Point out leukocytes.
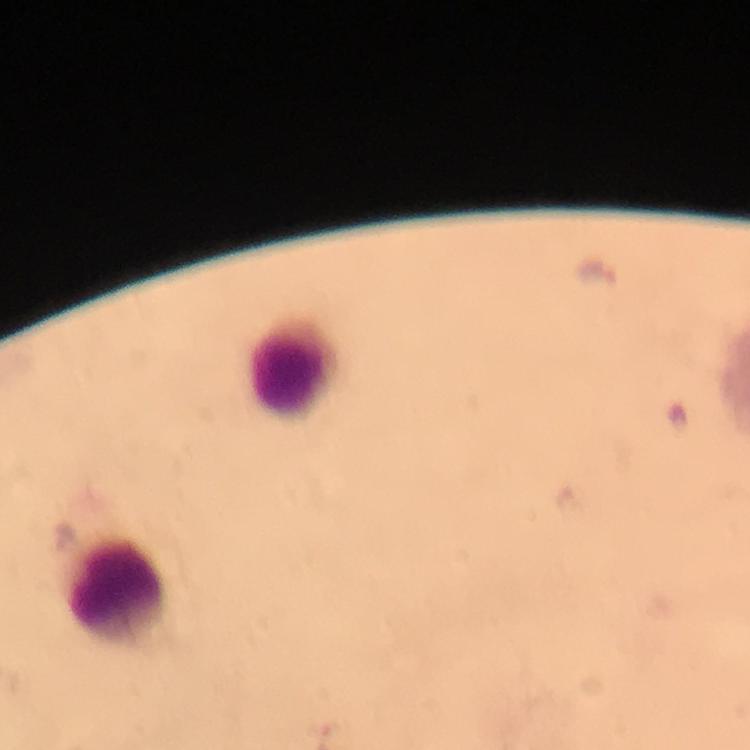
Approximate centers as {x, y} in pixels.
Leukocytes: {295, 367}, {114, 586}.

cropped from = one field of view
immersion oil = applied
magnification = 100x
preparation = thick blood film
image size = 750×750 pixels
stain = Giemsa
capture = smartphone mounted on the microscope
context = from a malaria diagnostic workup
malaria parasite locations = approximate centers as {x, y} in pixels: {597, 271}, {63, 537}